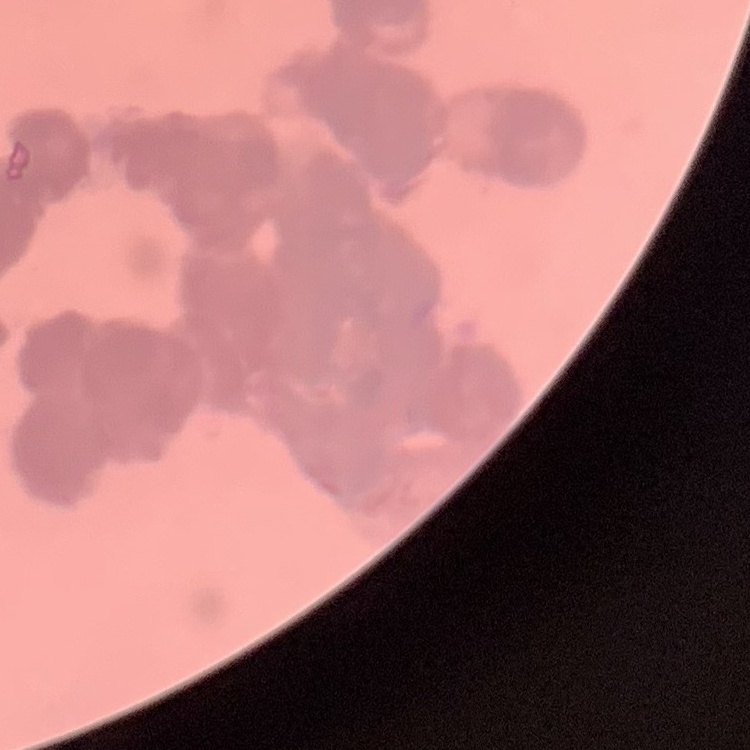
red blood cell morphology = rouleaux formation
stain = Field's or Giemsa
image type = square crop of a larger photomicrograph
preparation = thin blood smear